Report the malaria status of this cell.
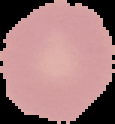

Uninfected.

Summary:
  - Preparation: thin blood smear
  - Image size: 115×124 pixels
  - Image type: segmented cell region on a black background